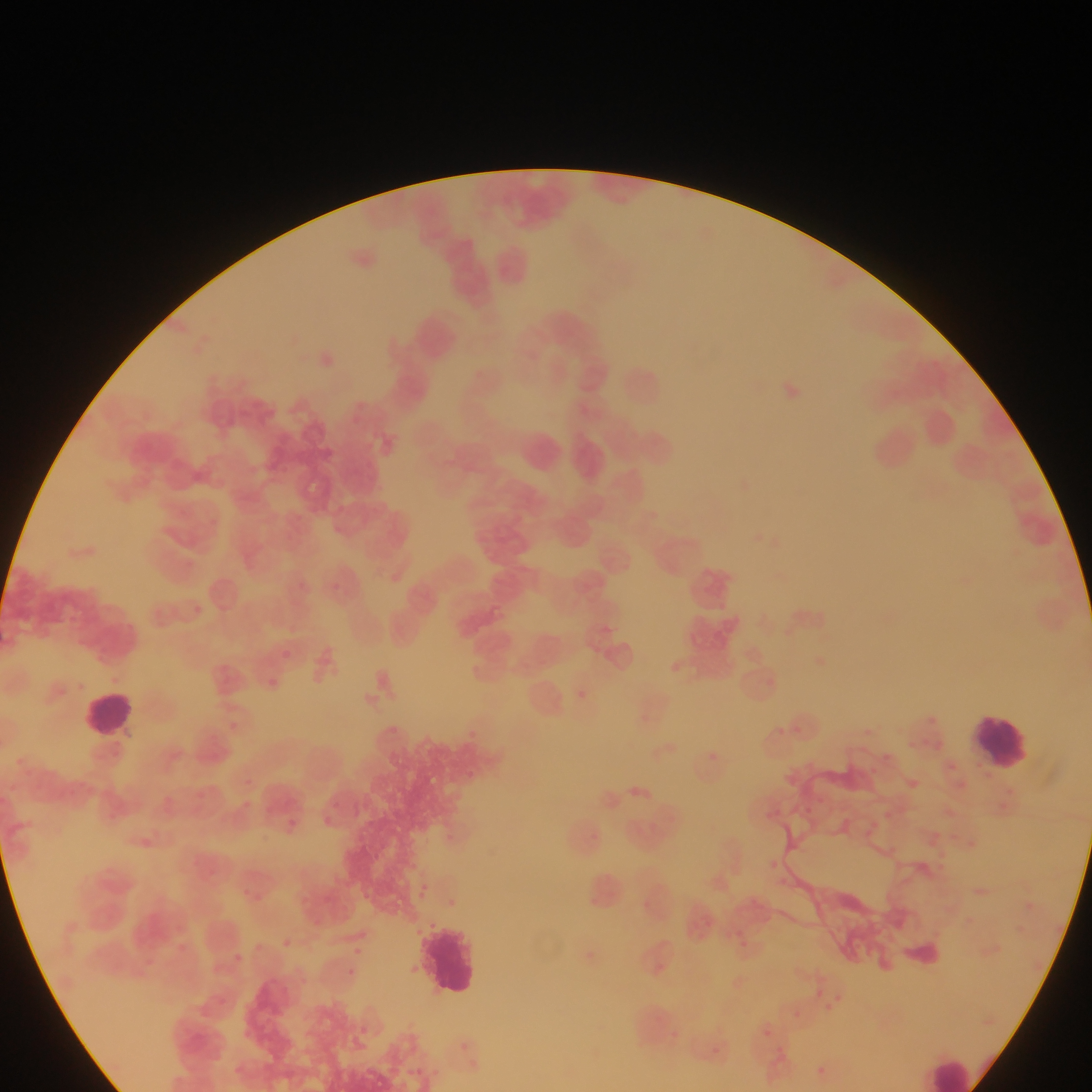
{
  "leukocyte_locations": "approximate bounding boxes as left top right bottom in pixels: 616 362 668 412; 520 431 566 479; 566 433 615 482; 77 688 140 741; 968 709 1036 776; 414 920 485 1001; 921 1048 979 1092",
  "malaria_parasite_locations": "approximate bounding boxes as left top right bottom in pixels: 261 673 285 695; 698 745 725 770; 623 779 659 810; 285 817 303 829; 131 832 160 858; 1017 896 1041 917; 731 934 758 958; 275 935 296 954; 343 965 360 981; 807 981 815 987; 832 984 851 1000; 821 1002 836 1018; 809 1061 830 1082",
  "image_size": "1092×1092 pixels",
  "field_of_view": "single",
  "capture": "mobile-phone photograph through a microscope",
  "preparation": "thin blood smear",
  "country": "Ghana"
}